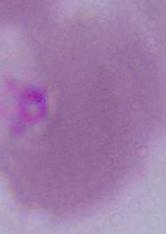
Micrograph. A red blood cell is seen. Captured at 1000x magnification.